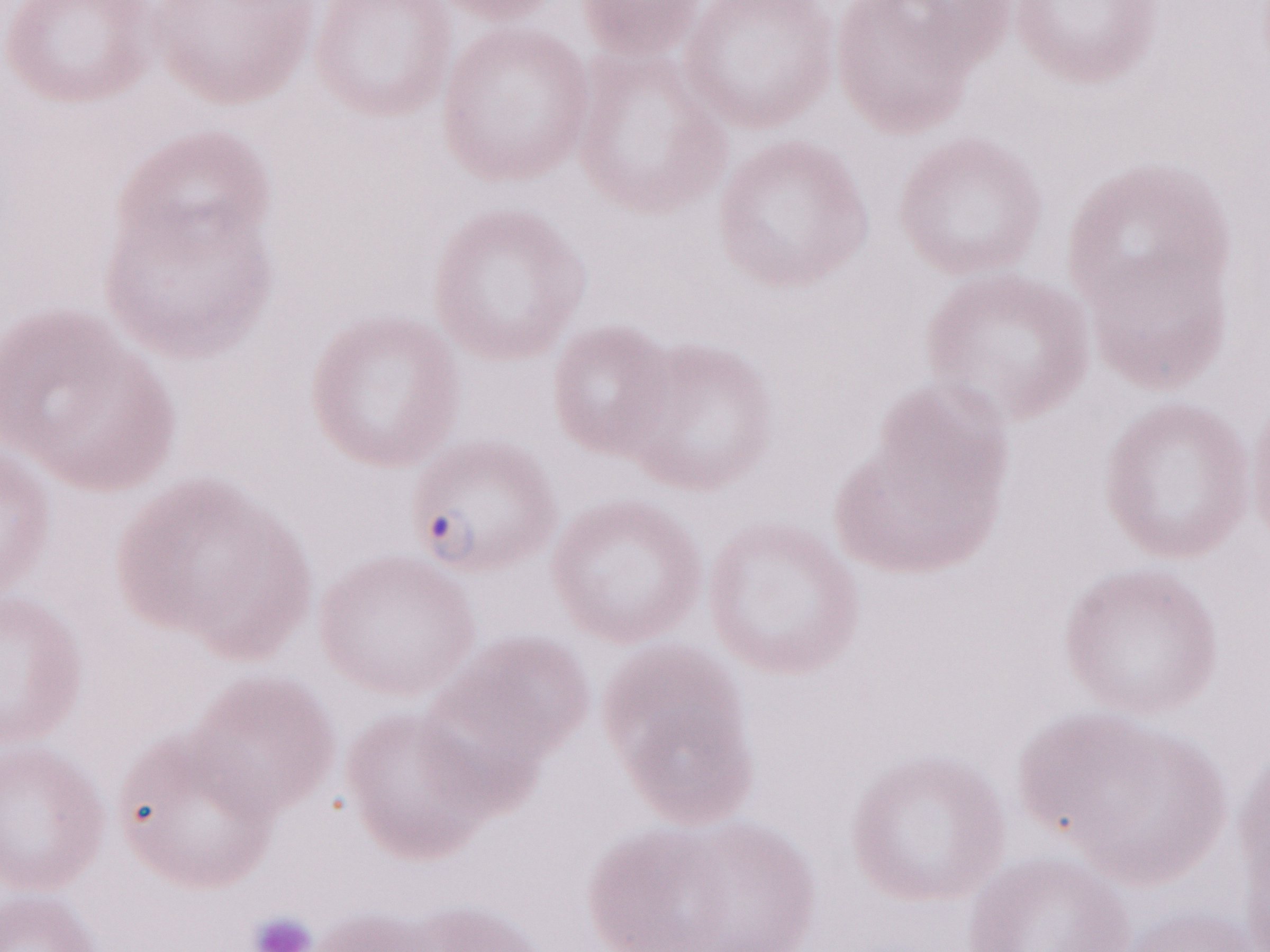

May-Grünwald-Giemsa (MGG) stain. Magnification: 1,000x. Patient-level malaria diagnosis: positive. Thin blood smear. Single field of view. Image is 1270×952 pixels. Olympus BX43 microscope and DP73 digital camera.